Name the cell type shown.
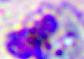

This is a leukocyte.

magnification = 400x
modality = micrograph